Report the malaria status of this cell.
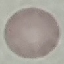

Uninfected.

Thin blood film. Cell patch, automatically extracted from a larger field of view and resized to 64 × 64 pixels. Acquired by smartphone through the microscope eyepiece. Giemsa stain.